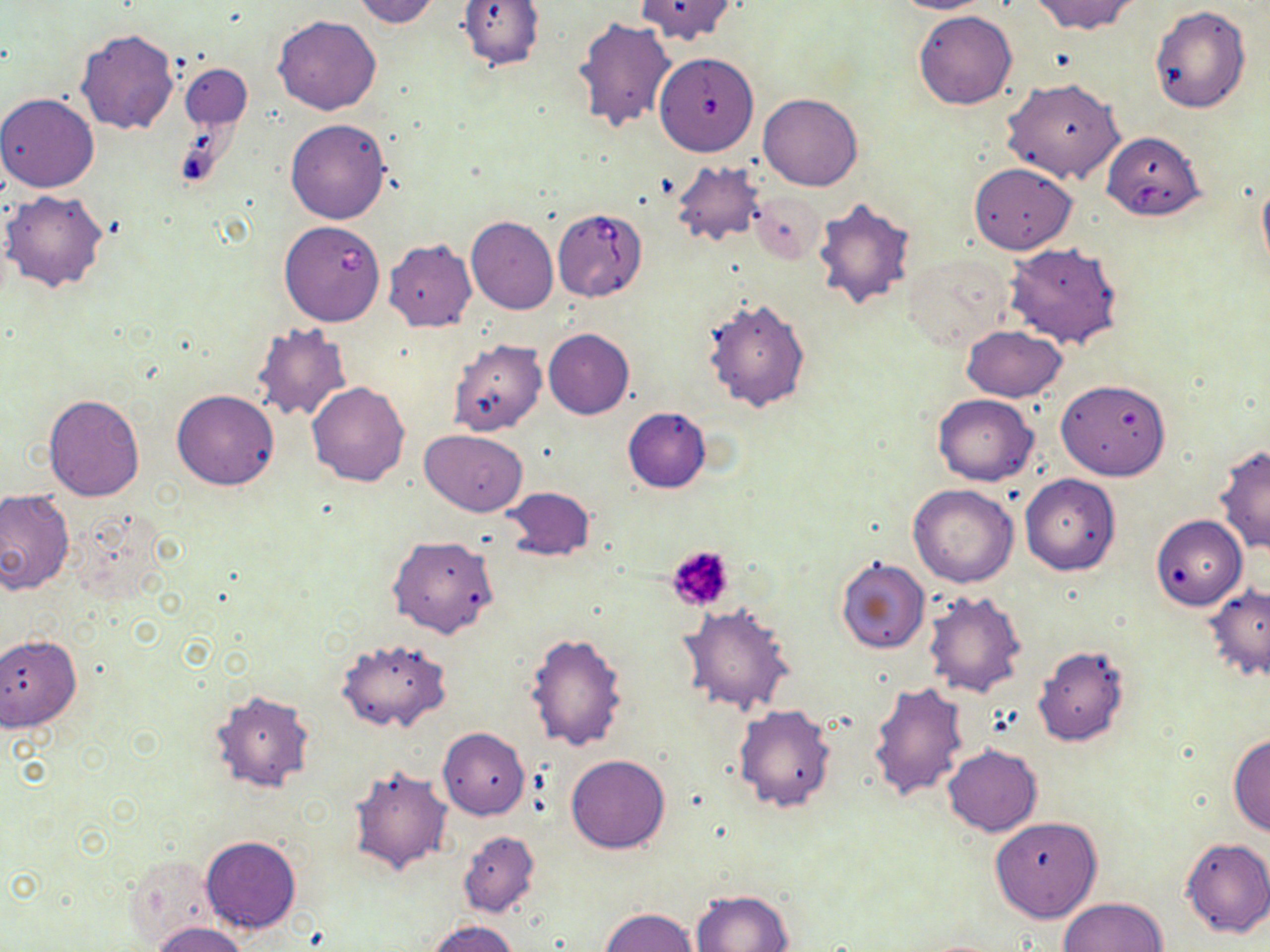 Approximate bounding boxes as named x1/y1/x2/y2 corners in pixels. Uninfected red blood cell locations: (x1=351, y1=0, x2=444, y2=27), (x1=455, y1=0, x2=544, y2=71), (x1=634, y1=0, x2=739, y2=44), (x1=891, y1=0, x2=993, y2=14), (x1=1030, y1=0, x2=1141, y2=36), (x1=1150, y1=5, x2=1251, y2=113), (x1=913, y1=10, x2=1016, y2=109), (x1=273, y1=16, x2=381, y2=115), (x1=573, y1=17, x2=678, y2=134), (x1=75, y1=29, x2=179, y2=134), (x1=654, y1=50, x2=759, y2=158), (x1=181, y1=63, x2=251, y2=131), (x1=1001, y1=78, x2=1125, y2=183), (x1=0, y1=92, x2=99, y2=193), (x1=758, y1=93, x2=862, y2=191), (x1=285, y1=118, x2=391, y2=223), (x1=670, y1=161, x2=763, y2=248), (x1=969, y1=163, x2=1077, y2=254), (x1=1257, y1=172, x2=1270, y2=277), (x1=749, y1=189, x2=825, y2=264), (x1=2, y1=190, x2=110, y2=293), (x1=811, y1=197, x2=919, y2=310), (x1=466, y1=216, x2=558, y2=314), (x1=384, y1=239, x2=477, y2=331), (x1=1004, y1=241, x2=1123, y2=349), (x1=906, y1=251, x2=1016, y2=351), (x1=702, y1=297, x2=812, y2=413), (x1=250, y1=322, x2=355, y2=423), (x1=962, y1=324, x2=1066, y2=402), (x1=543, y1=329, x2=635, y2=419), (x1=449, y1=338, x2=548, y2=437), (x1=1056, y1=378, x2=1170, y2=480), (x1=307, y1=381, x2=409, y2=485), (x1=172, y1=390, x2=279, y2=490), (x1=43, y1=393, x2=145, y2=501), (x1=932, y1=394, x2=1039, y2=485), (x1=623, y1=407, x2=711, y2=493), (x1=419, y1=429, x2=527, y2=516), (x1=1215, y1=446, x2=1269, y2=555), (x1=1020, y1=473, x2=1121, y2=575), (x1=908, y1=483, x2=1018, y2=587), (x1=502, y1=486, x2=594, y2=562), (x1=0, y1=491, x2=73, y2=596), (x1=1150, y1=514, x2=1248, y2=610), (x1=387, y1=534, x2=498, y2=638), (x1=835, y1=558, x2=930, y2=655), (x1=1202, y1=582, x2=1270, y2=685), (x1=922, y1=590, x2=1026, y2=697), (x1=678, y1=605, x2=796, y2=716), (x1=526, y1=631, x2=629, y2=752), (x1=0, y1=633, x2=81, y2=733), (x1=337, y1=638, x2=448, y2=732), (x1=1032, y1=645, x2=1130, y2=747), (x1=868, y1=680, x2=969, y2=801), (x1=208, y1=688, x2=315, y2=794), (x1=735, y1=704, x2=836, y2=813), (x1=438, y1=726, x2=530, y2=819), (x1=1229, y1=734, x2=1270, y2=837), (x1=942, y1=744, x2=1043, y2=836), (x1=566, y1=754, x2=671, y2=854), (x1=349, y1=763, x2=453, y2=875), (x1=989, y1=815, x2=1101, y2=923), (x1=458, y1=829, x2=539, y2=918), (x1=200, y1=836, x2=300, y2=933), (x1=1181, y1=837, x2=1270, y2=939), (x1=125, y1=853, x2=221, y2=946), (x1=692, y1=889, x2=794, y2=951), (x1=1057, y1=897, x2=1168, y2=952), (x1=601, y1=907, x2=698, y2=952), (x1=426, y1=918, x2=519, y2=952), (x1=152, y1=922, x2=250, y2=952). Babesia divergens-infected red blood cell locations: (x1=1102, y1=137, x2=1208, y2=220), (x1=552, y1=208, x2=648, y2=302), (x1=279, y1=220, x2=386, y2=326). Platelet locations: (x1=665, y1=544, x2=737, y2=614). Slide-level diagnosis: Babesia divergens. Thin blood smear. May-Grünwald-Giemsa-stained preparation. 1000x magnification. Image is 1270×952 pixels. Optical microscopy. One field of a larger specimen.